Outline each uninfected red blood cell.
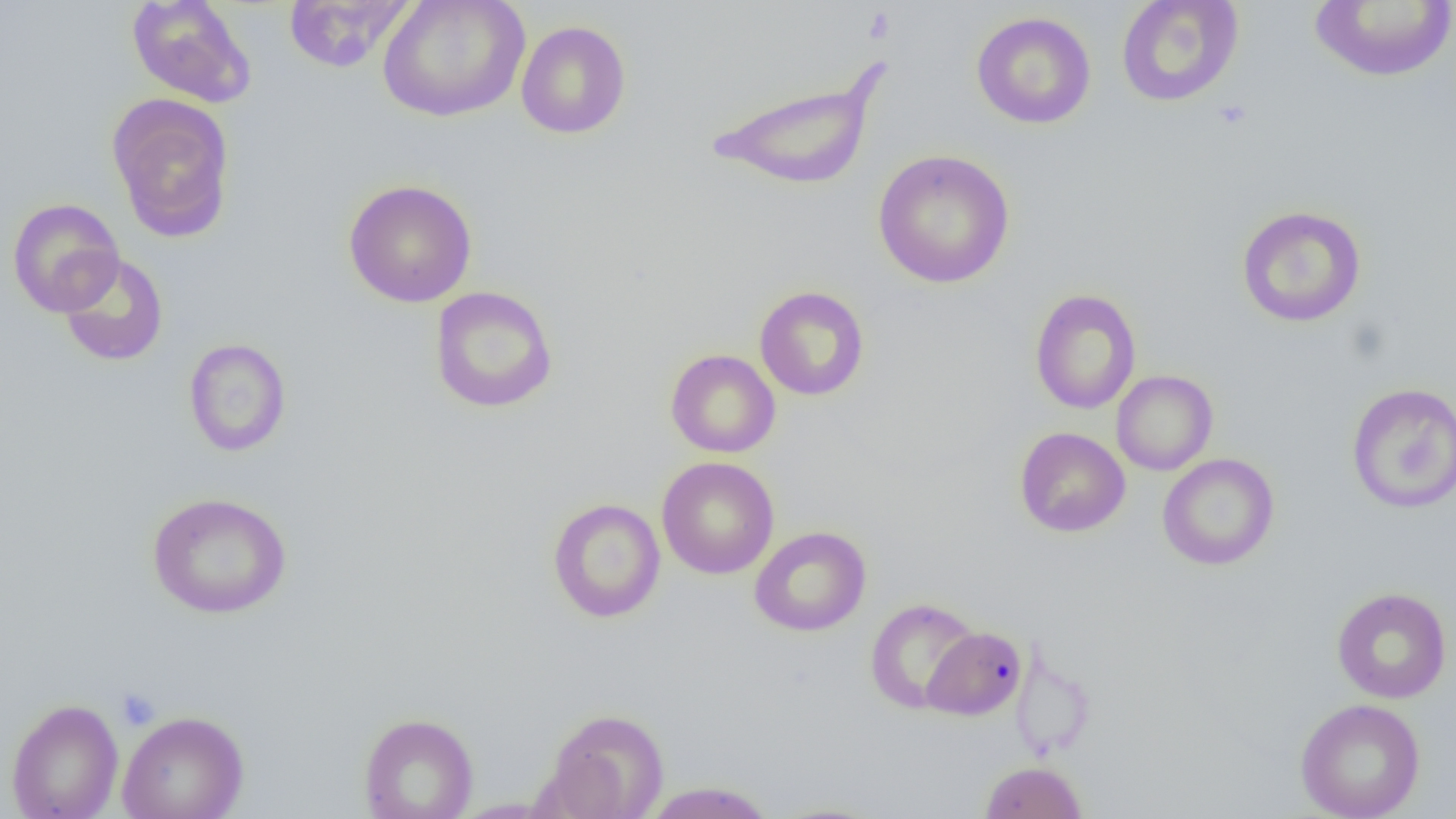

Approximate bounding boxes as [x1, y1, x2, y2] in pixels.
Uninfected red blood cells: [126, 0, 256, 108], [377, 0, 531, 122], [1115, 0, 1245, 107], [283, 1, 414, 73], [1309, 1, 1456, 82], [971, 11, 1096, 129], [516, 20, 631, 139], [706, 63, 888, 192], [106, 94, 236, 242], [873, 149, 1015, 289], [343, 179, 477, 308], [7, 197, 124, 317], [1236, 205, 1367, 327], [56, 252, 169, 367], [754, 285, 870, 401], [428, 286, 559, 414], [1029, 288, 1142, 414], [183, 337, 292, 457], [665, 349, 780, 458], [1111, 370, 1218, 475], [1346, 382, 1456, 513], [1015, 426, 1130, 537], [1157, 453, 1280, 571], [656, 456, 779, 579], [147, 491, 292, 619], [547, 497, 666, 623], [749, 526, 871, 636], [1331, 587, 1452, 704], [864, 597, 981, 714], [922, 626, 1028, 721], [6, 698, 123, 819], [1295, 698, 1426, 819], [543, 707, 670, 819], [117, 710, 250, 819], [358, 712, 479, 819], [979, 760, 1088, 819], [640, 781, 777, 819], [761, 801, 893, 819].

Platelet locations: [116, 688, 161, 730]. Slide-level diagnosis: negative for blood parasites. Image is 1456×819 pixels. Thin blood film. One field of a larger specimen. Optical microscopy. Captured at 1000x magnification.